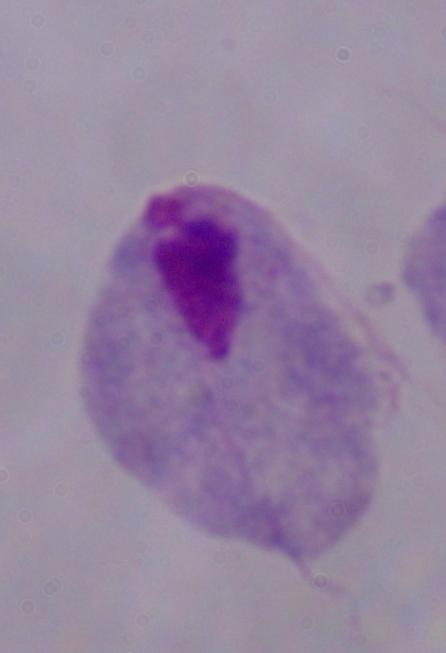
modality = micrograph
magnification = 1000x
identification = trichomonad